Comment on the morphology of the red blood cells.
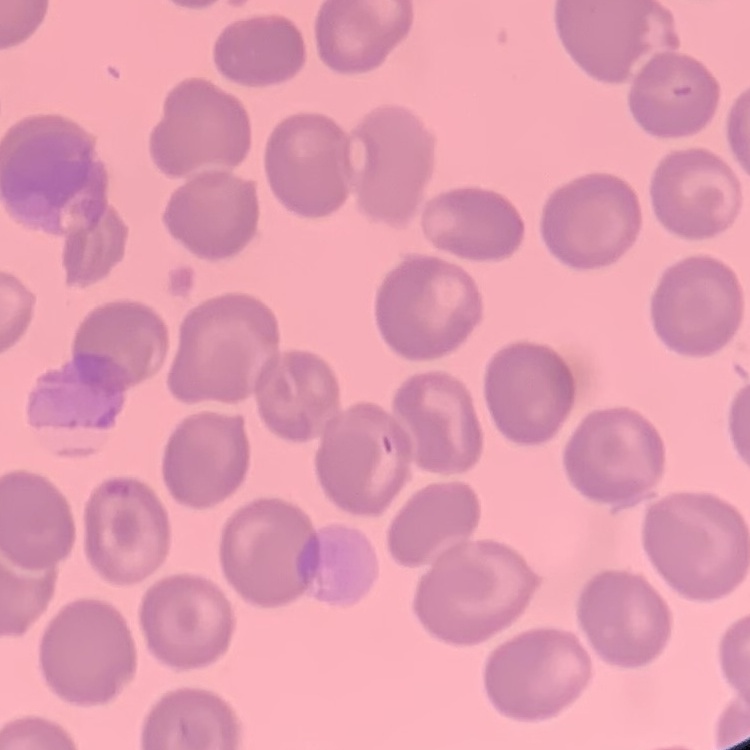

No rouleaux formation.

Summary:
  - Preparation: thin peripheral smear
  - Stain: Field's or Giemsa
  - Image type: square crop of a larger photomicrograph